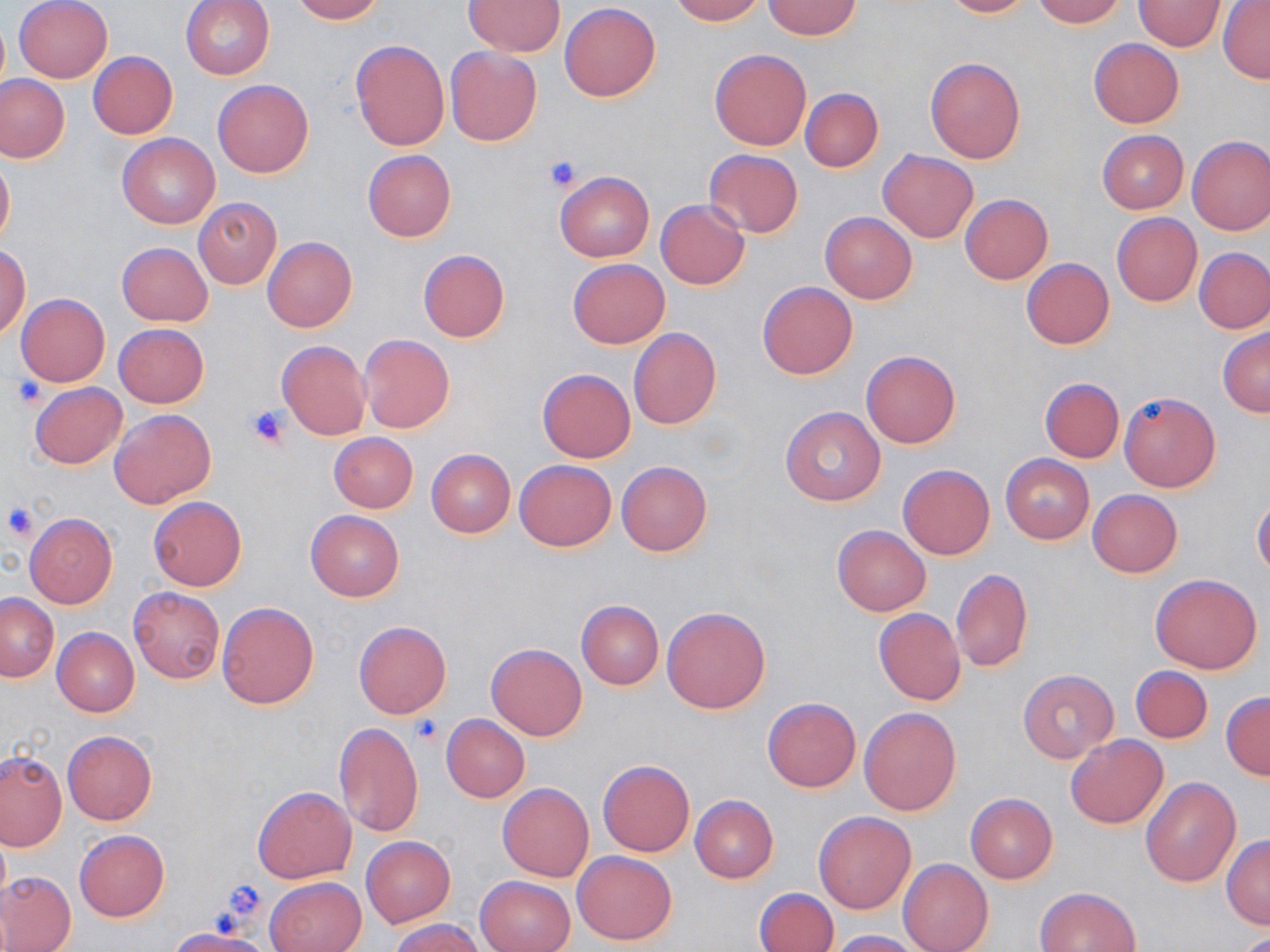 Approximate bounding boxes as (x1, y1, x2, y2) in pixels. Platelet locations: (544, 154, 585, 191), (8, 376, 46, 409), (244, 403, 292, 449), (2, 499, 39, 541), (410, 714, 444, 746), (218, 881, 268, 923). Uninfected red blood cell locations: (14, 0, 112, 84), (180, 0, 275, 80), (289, 0, 384, 23), (670, 0, 765, 24), (762, 0, 861, 40), (941, 0, 1034, 18), (465, 1, 565, 55), (1031, 1, 1126, 27), (1133, 1, 1228, 50), (1218, 1, 1270, 84), (560, 3, 660, 101), (351, 39, 449, 150), (1089, 39, 1184, 128), (445, 46, 542, 145), (709, 48, 812, 150), (89, 52, 177, 138), (925, 56, 1026, 163), (0, 76, 69, 162), (212, 79, 315, 178), (800, 87, 883, 171), (1098, 130, 1188, 213), (116, 132, 219, 228), (1187, 135, 1270, 235), (877, 148, 979, 242), (703, 149, 804, 238), (362, 150, 456, 241), (0, 153, 15, 249), (554, 171, 654, 262), (960, 194, 1051, 284), (194, 197, 281, 289), (656, 200, 749, 289), (821, 211, 916, 304), (1112, 212, 1201, 306), (262, 236, 357, 333), (116, 242, 213, 326), (0, 243, 31, 340), (1195, 247, 1270, 334), (418, 249, 510, 342), (1021, 258, 1113, 349), (568, 259, 670, 348), (758, 281, 857, 379), (16, 293, 110, 386), (115, 324, 208, 407), (628, 328, 721, 429), (1218, 328, 1270, 418), (359, 334, 455, 433), (276, 339, 371, 441), (861, 349, 961, 449), (538, 368, 636, 462), (1040, 377, 1124, 462), (30, 382, 127, 469), (1120, 391, 1220, 492), (779, 407, 886, 505), (109, 408, 216, 508), (328, 433, 418, 512), (426, 449, 515, 537), (1000, 454, 1095, 543), (515, 460, 616, 551), (616, 461, 712, 557), (898, 462, 995, 560), (1087, 489, 1183, 578), (147, 495, 247, 591), (1253, 497, 1270, 580), (304, 510, 404, 602), (25, 513, 117, 608), (832, 524, 931, 616), (951, 569, 1033, 672), (1151, 573, 1264, 673), (129, 586, 225, 683), (0, 594, 58, 682), (576, 600, 664, 690), (217, 602, 318, 709), (662, 606, 770, 714), (873, 609, 965, 706), (353, 620, 451, 718), (53, 627, 139, 717), (486, 643, 587, 740), (1131, 665, 1212, 743), (1018, 669, 1117, 762), (1221, 690, 1270, 780), (763, 697, 860, 792), (860, 706, 961, 815), (442, 715, 529, 802), (333, 722, 424, 838), (62, 730, 157, 825), (1066, 734, 1168, 829), (1, 751, 66, 851), (597, 759, 695, 857), (1140, 776, 1242, 886), (497, 781, 595, 881), (253, 786, 356, 883), (965, 792, 1058, 883), (690, 795, 778, 883), (813, 809, 917, 914), (0, 825, 11, 919), (74, 830, 169, 921), (1222, 834, 1270, 929), (361, 836, 455, 927), (572, 850, 677, 945), (898, 858, 993, 952), (0, 872, 76, 952), (476, 875, 574, 952), (264, 876, 365, 952), (1034, 886, 1141, 952), (755, 888, 837, 952), (391, 919, 483, 952), (165, 928, 276, 952), (830, 929, 926, 952). Slide-level diagnosis: negative for blood parasites. Single field of view. May-Grünwald-Giemsa-stained preparation. Image is 1270×952 pixels. Thin blood smear. Light microscopy. Captured at 1000x magnification.